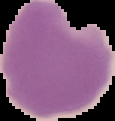
Summary:
  - Image type: cell region segmented out of the field of view; surrounding area masked to black
  - Result: negative for malaria parasites
  - Image size: 115×121 pixels
  - Preparation: thin blood film